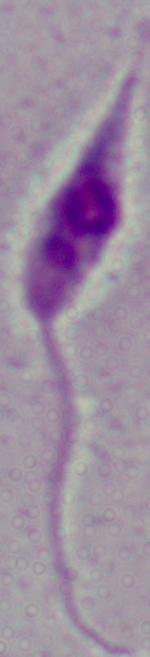
A Leishmania parasite is seen. Photomicrograph. 1000x magnification.